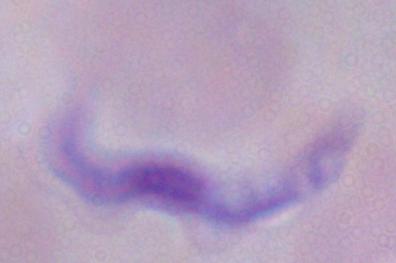 Photomicrograph. A trypanosome is shown. 1000x magnification.